Comment on the morphology of the erythrocytes.
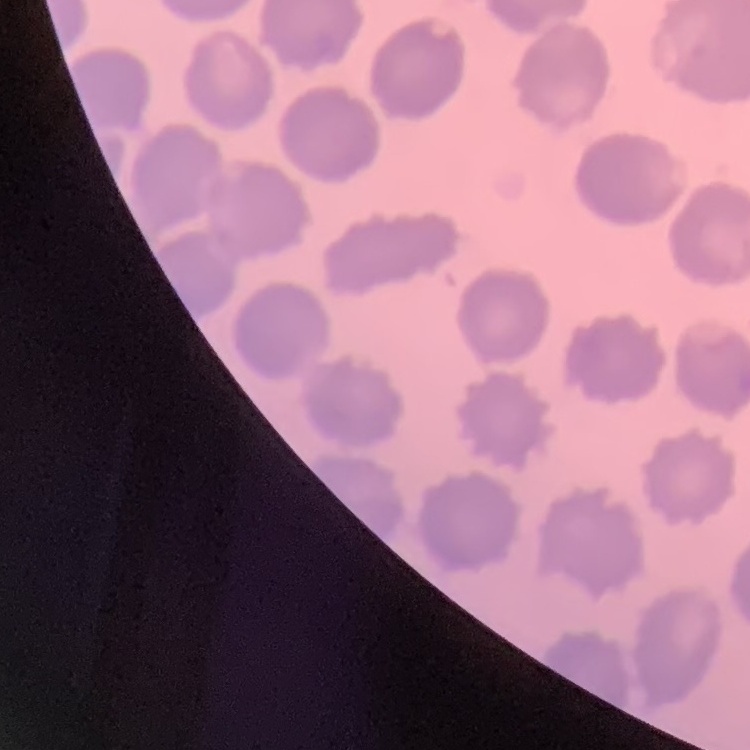
No rouleaux formation.

Summary:
  - Stain: Field's or Giemsa
  - Image type: square crop of a larger photomicrograph
  - Preparation: thin blood smear